Describe the morphology of the red blood cells.
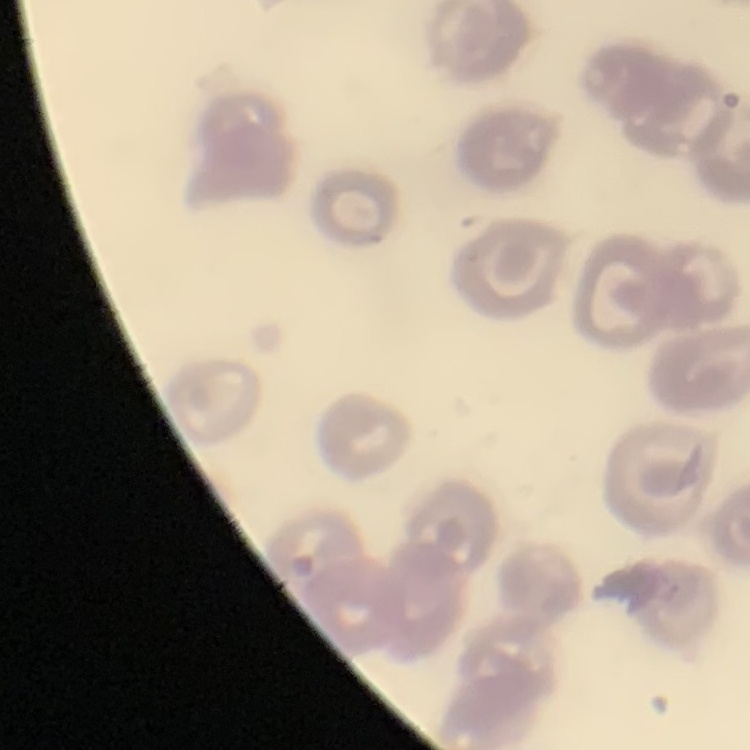

They show no rouleaux formation.

Square crop of a larger photomicrograph. Thin blood smear. Stained with either Field's or Giemsa.